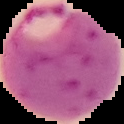
{
  "malaria_status": "parasitized",
  "image_size": "124×124 pixels",
  "image_type": "segmented cell region on a black background",
  "preparation": "thin blood smear"
}